State which parasite is depicted.
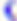

Toxoplasma gondii.

Photomicrograph. 400x magnification.